Classify this cell by malaria status.
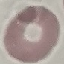
Uninfected.

Summary:
  - Stain: Giemsa
  - Image type: automatically extracted cell patch, resized to 64 × 64 pixels
  - Capture: smartphone through the microscope eyepiece
  - Preparation: thin blood film